Classify this cell by malaria status.
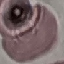

It is uninfected.

capture: smartphone camera at the microscope eyepiece
image_type: cell patch, automatically extracted from a larger field of view and resized to 64 × 64 pixels
preparation: thin blood film
stain: Giemsa